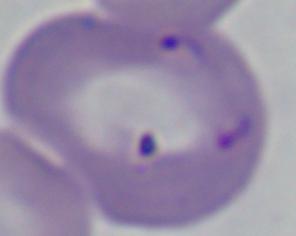

1000x magnification. Photomicrograph. A Babesia parasite is shown.